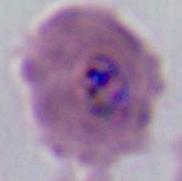

Summary:
  - Magnification: 400x or 1000x
  - Identification: Plasmodium
  - Modality: photomicrograph